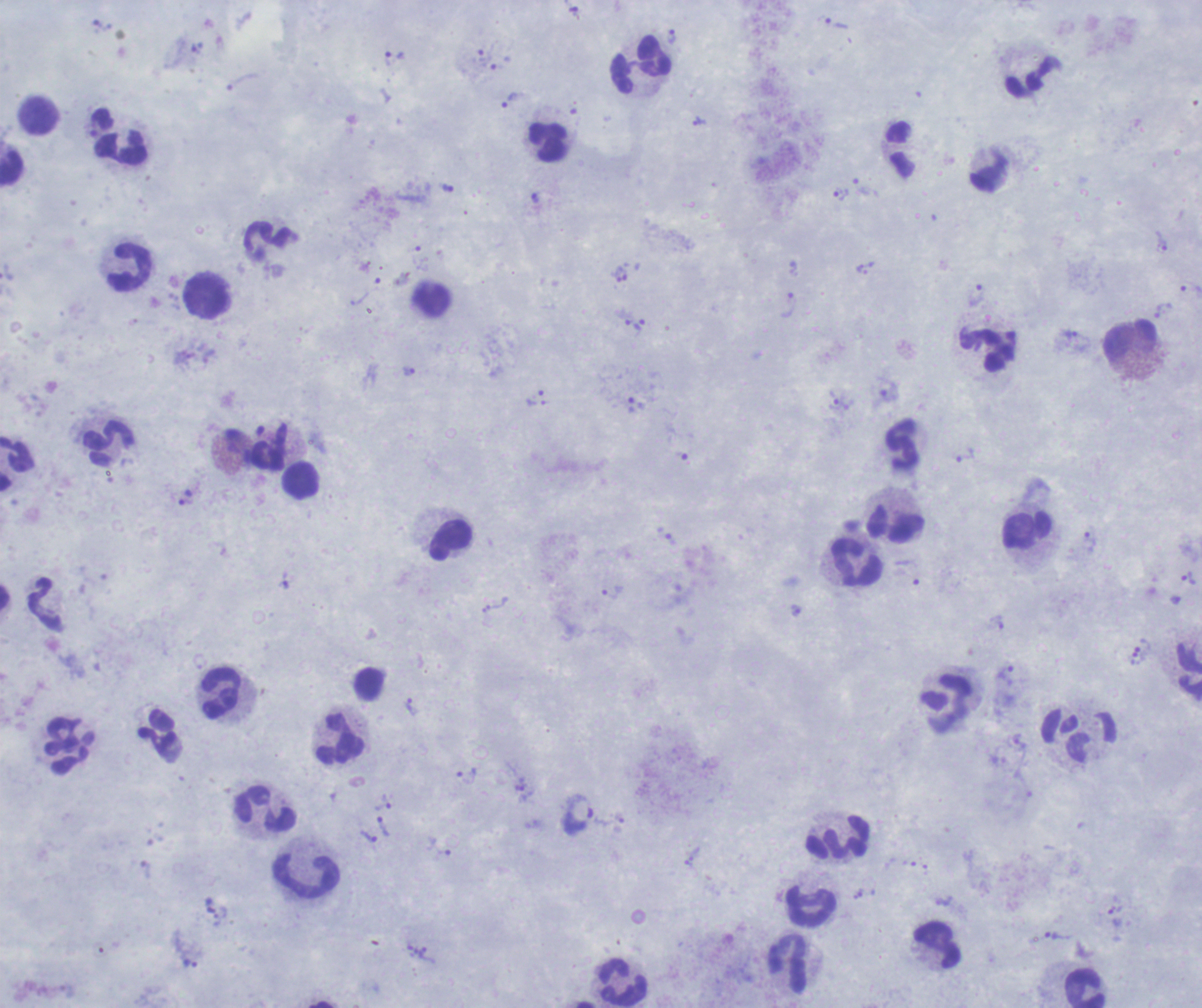

One field from this slide. Image is 1202×1008 pixels. Romanowsky-stained preparation. Thick smear of blood.